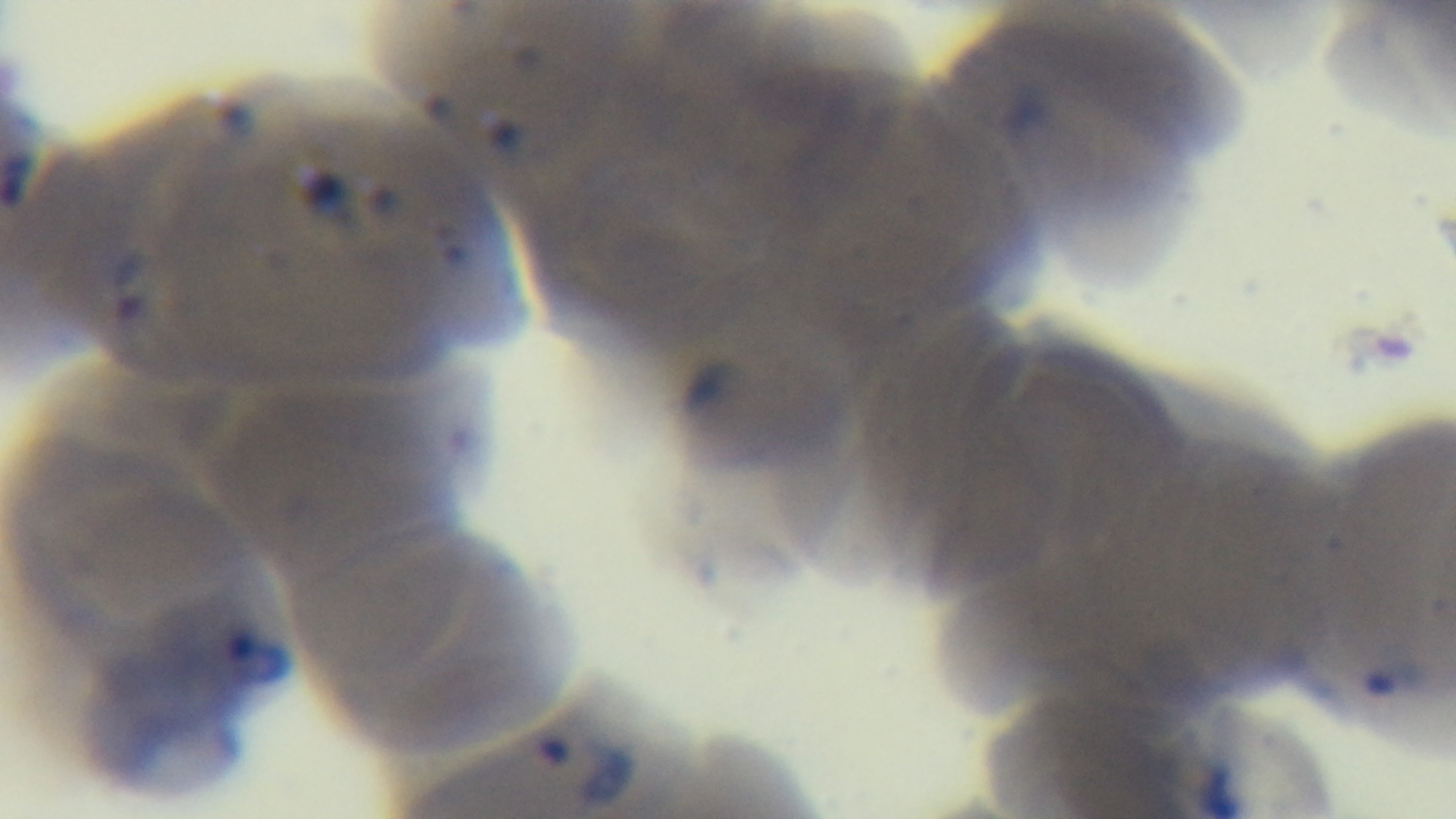
field of view = one from the slide
objective = 100x oil immersion
stain = Giemsa
capture = mounted 4K digital camera
modality = light microscopy
malaria status = infected
preparation = thin